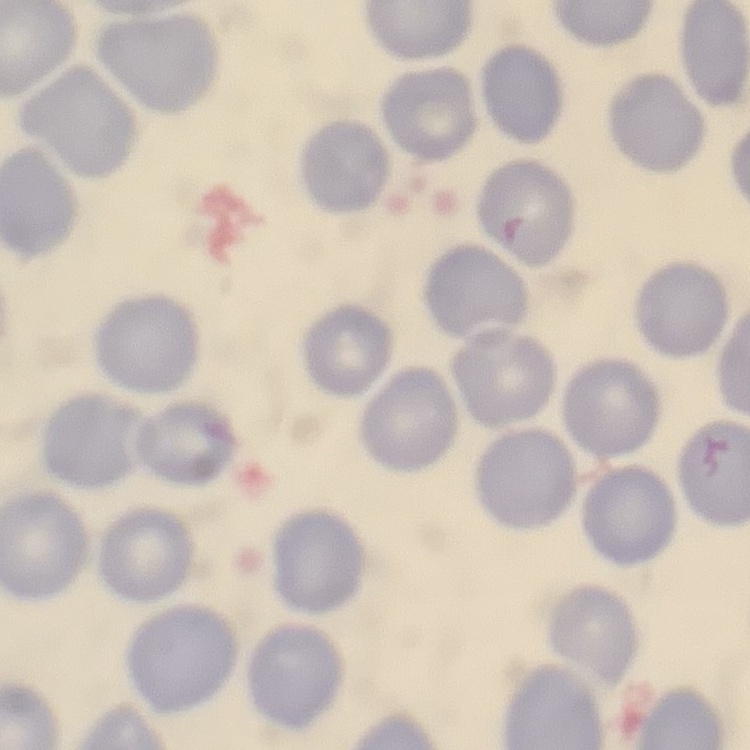

red blood cell morphology = no rouleaux formation
stain = Field's or Giemsa
image type = square crop of a larger photomicrograph
preparation = thin blood film